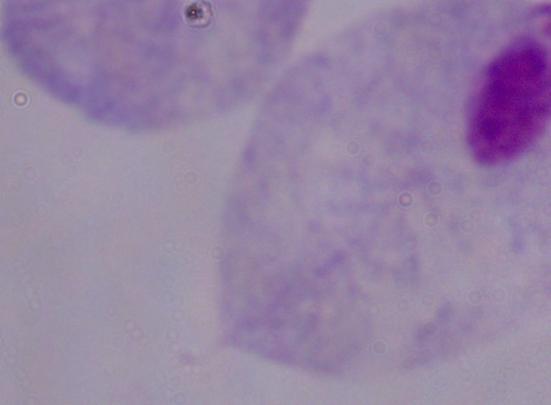 Micrograph. 1000x magnification. A trichomonad is seen.